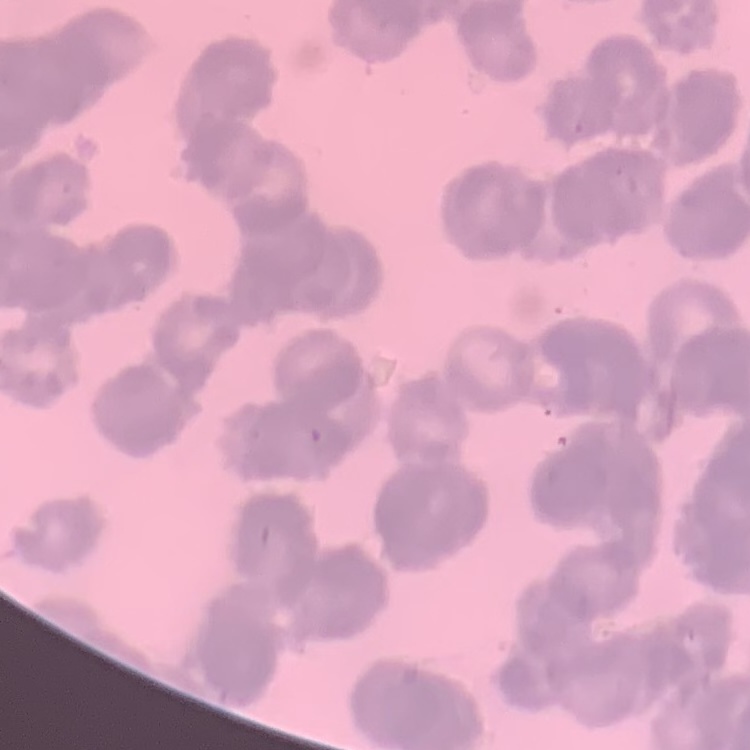

{
  "erythrocyte_morphology": "rouleaux formation",
  "preparation": "thin blood film",
  "stain": "Field's or Giemsa",
  "image_type": "one tile cut from a larger photomicrograph"
}